Assess this cell for malaria.
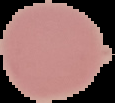

Uninfected.

Image is 115×103 pixels. Cell region segmented out of the field of view; the surrounding area is masked to black. From a thin blood film.